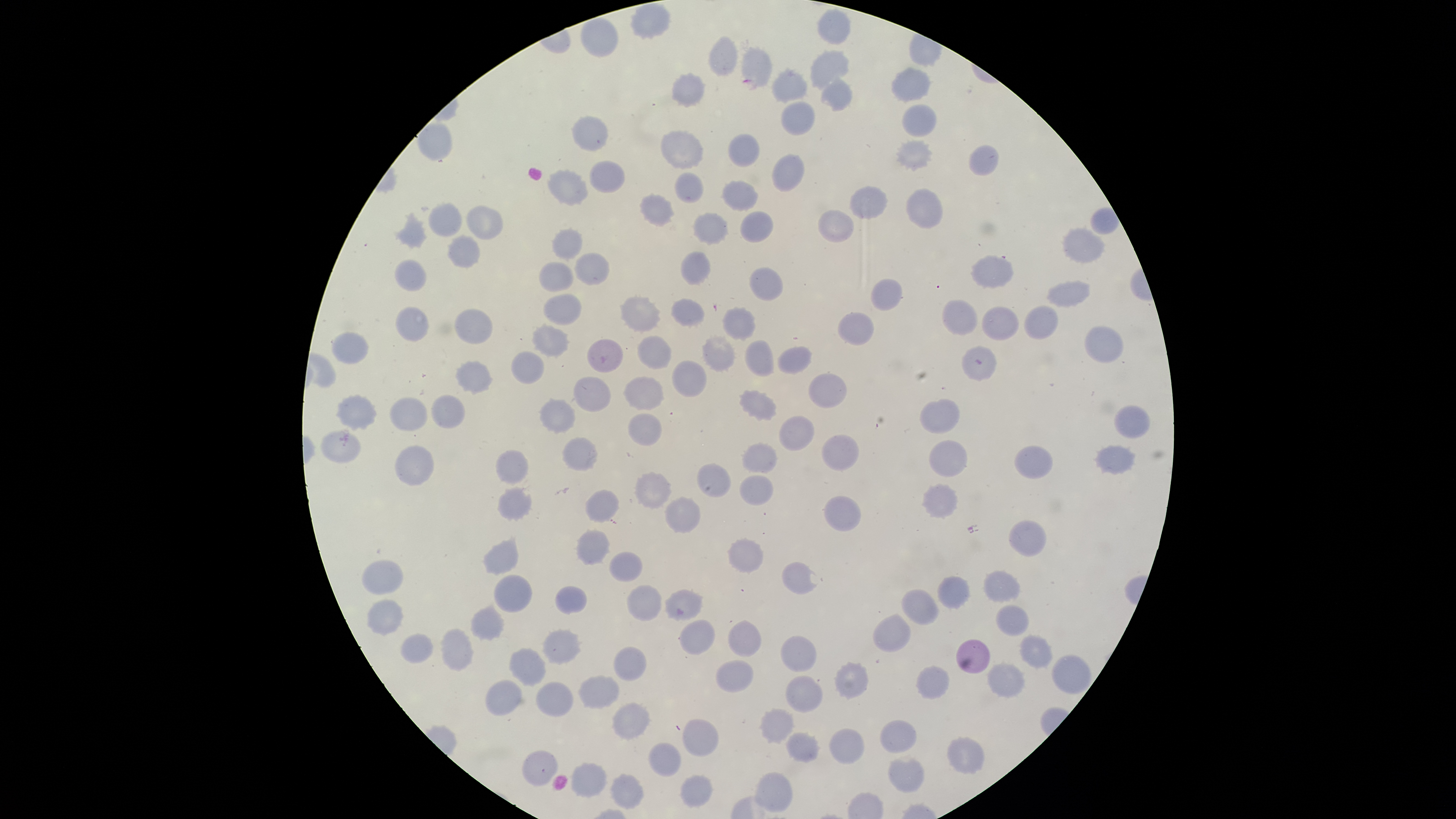

{
  "visible_region": "circular",
  "preparation": "thin blood smear",
  "parasitized_RBCs": "approximate bounding boxes as [left, top, right, bottom] in pixels: [740, 45, 773, 90]",
  "image_size": "1456×819 pixels",
  "capture": "smartphone photograph through the microscope eyepiece",
  "field_of_view": "single",
  "presence": "malaria parasites identified",
  "stain": "Giemsa",
  "species": "Plasmodium falciparum",
  "uninfected_RBCs": "approximate bounding boxes as [left, top, right, bottom] in pixels: [629, 2, 670, 36], [819, 10, 848, 43], [581, 17, 618, 57], [710, 38, 737, 74], [811, 51, 850, 89], [891, 68, 930, 103], [772, 70, 806, 103], [671, 74, 705, 106], [822, 78, 852, 108], [780, 101, 814, 136], [902, 106, 935, 136], [571, 116, 607, 151], [416, 121, 452, 160], [660, 131, 704, 168], [728, 134, 759, 168], [896, 142, 931, 169], [969, 146, 998, 177], [772, 154, 804, 193], [590, 159, 625, 192], [548, 169, 588, 206], [675, 172, 703, 203], [722, 181, 758, 212], [851, 186, 888, 219], [907, 187, 942, 228], [641, 192, 674, 226], [428, 204, 462, 236], [467, 205, 503, 241], [818, 209, 854, 242], [692, 212, 728, 244], [740, 212, 773, 242], [396, 214, 427, 247], [1062, 228, 1105, 263], [552, 230, 584, 258], [447, 235, 481, 267], [574, 252, 609, 284], [681, 252, 710, 285], [972, 255, 1013, 286], [394, 260, 426, 291], [539, 262, 573, 292], [750, 267, 782, 301], [872, 279, 902, 309], [1046, 281, 1091, 308], [544, 296, 583, 325], [621, 296, 660, 332], [672, 297, 704, 327], [944, 300, 977, 334], [1025, 305, 1059, 339], [982, 306, 1019, 340], [396, 307, 429, 341], [722, 308, 754, 341], [454, 310, 492, 344], [840, 313, 874, 345], [534, 325, 568, 357], [1086, 326, 1124, 364], [333, 332, 369, 363], [703, 335, 735, 372], [639, 337, 672, 368], [587, 339, 622, 372], [745, 341, 774, 377], [963, 346, 997, 382], [778, 347, 812, 373], [511, 350, 544, 384], [672, 360, 707, 397], [457, 361, 491, 393], [809, 373, 847, 407], [573, 376, 612, 413], [625, 377, 664, 408], [738, 391, 777, 418], [432, 393, 465, 429], [338, 396, 376, 428], [390, 397, 429, 431], [541, 399, 576, 432], [921, 399, 960, 435], [1116, 406, 1151, 438], [630, 412, 664, 446], [781, 417, 815, 450], [322, 431, 361, 461], [822, 435, 859, 471], [563, 437, 599, 472], [930, 439, 967, 476], [394, 444, 434, 486], [744, 444, 777, 472], [1094, 444, 1136, 474], [1014, 446, 1053, 479], [496, 451, 528, 483], [698, 463, 731, 497], [635, 472, 672, 507], [740, 475, 773, 505], [922, 485, 959, 518], [498, 487, 531, 518], [586, 490, 620, 522], [826, 495, 862, 530], [666, 499, 700, 533], [1010, 519, 1048, 556], [577, 531, 610, 565], [730, 539, 762, 573], [483, 541, 519, 574], [609, 552, 643, 581], [361, 559, 404, 595], [782, 562, 818, 594], [983, 572, 1019, 602], [493, 574, 533, 614], [939, 578, 970, 609], [556, 585, 589, 613], [628, 585, 661, 621], [902, 589, 938, 625], [666, 591, 703, 618], [368, 600, 403, 633], [997, 605, 1029, 637], [472, 606, 505, 641], [872, 613, 913, 651], [680, 619, 715, 653], [729, 619, 761, 657], [441, 629, 473, 671], [401, 632, 434, 662], [544, 632, 580, 663], [1021, 636, 1052, 668], [781, 637, 816, 673], [957, 639, 990, 673], [613, 647, 646, 681], [511, 650, 544, 685], [1053, 653, 1091, 695], [716, 659, 754, 692], [987, 662, 1025, 698], [835, 664, 868, 699], [917, 667, 949, 699], [579, 676, 621, 708], [787, 676, 823, 712], [486, 679, 521, 714], [537, 681, 572, 716], [614, 703, 651, 739], [763, 708, 796, 741], [683, 719, 719, 757], [880, 722, 918, 753], [830, 728, 864, 764], [788, 732, 819, 761], [948, 738, 984, 775], [650, 744, 681, 778], [523, 750, 558, 787], [888, 758, 924, 793], [572, 763, 606, 798], [756, 772, 793, 813], [612, 774, 643, 810], [680, 776, 711, 808]"
}